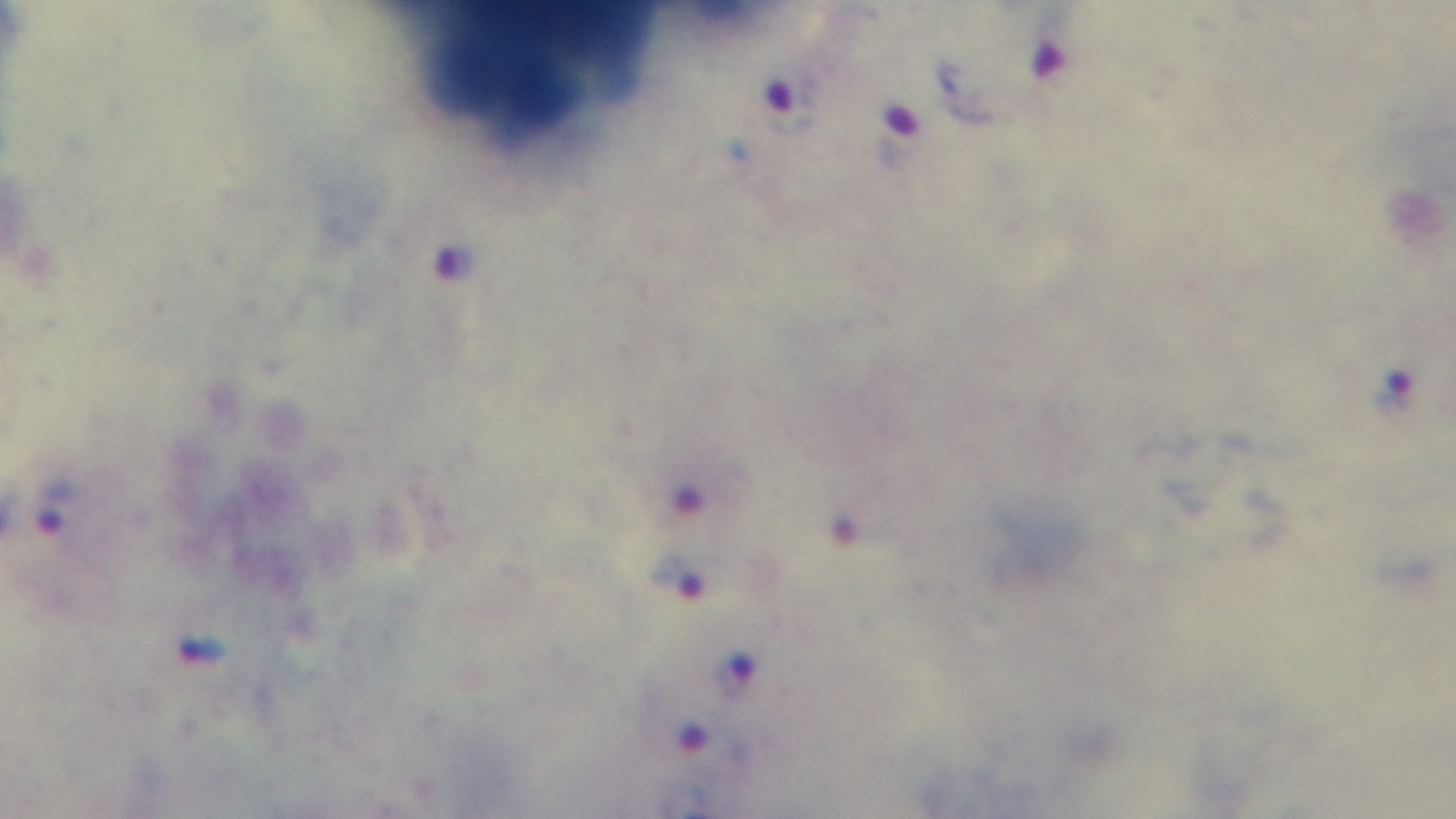

objective: 100x oil immersion
field_of_view: single
stain: Giemsa
preparation: thick blood film
capture: mounted 4K digital camera
modality: light microscopy
malaria_status: infected